Give the extent of all uninfected red blood cells.
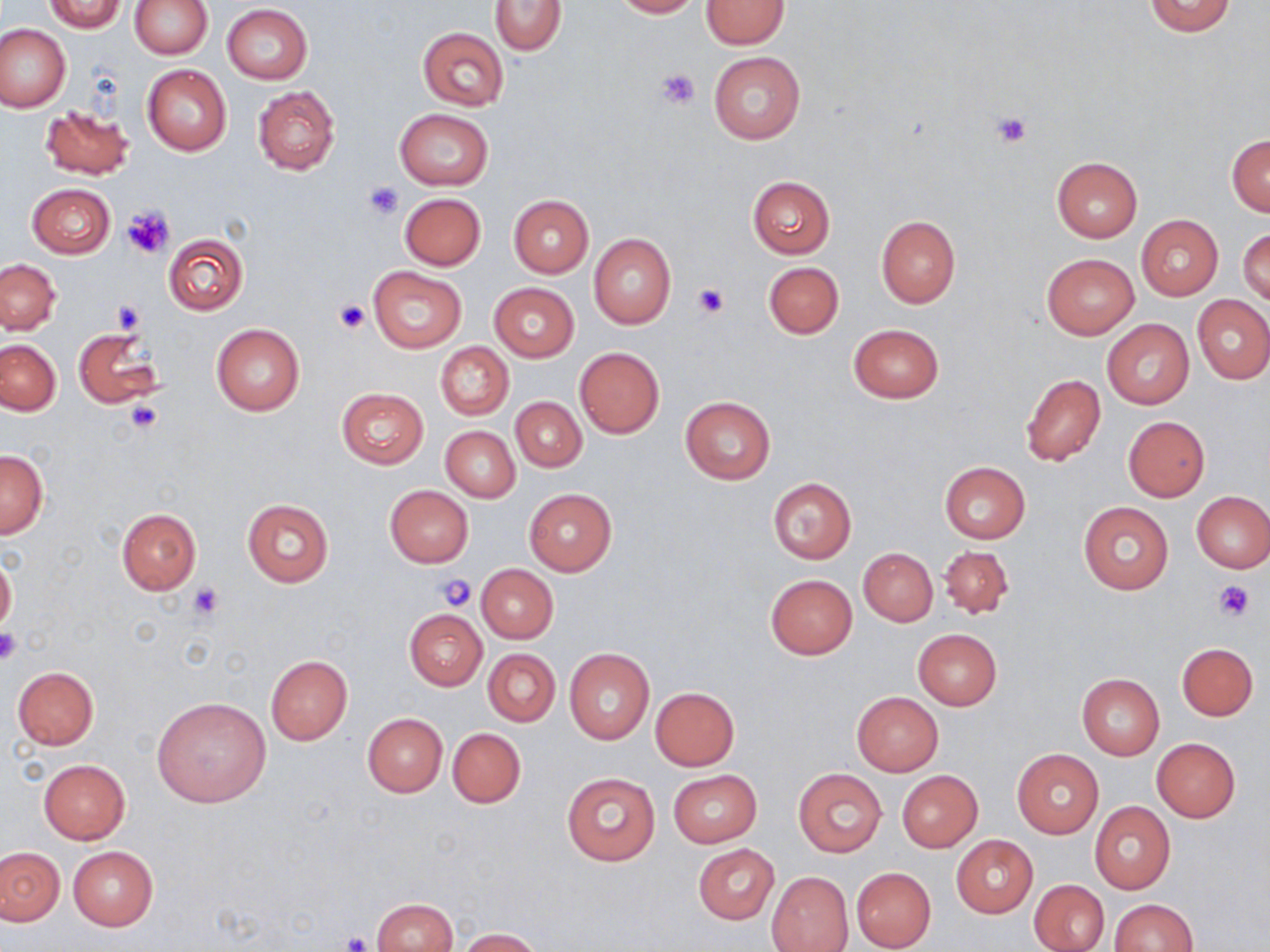
Approximate bounding boxes as (x1,y1)-(x2,y2) corner pairs in pixels.
Uninfected red blood cells: (131,0)-(212,59), (612,0)-(701,18), (40,1)-(126,32), (491,1)-(568,54), (700,1)-(788,49), (1143,1)-(1236,37), (221,4)-(312,84), (0,23)-(70,113), (417,26)-(509,111), (709,52)-(805,145), (142,65)-(232,156), (253,86)-(339,174), (38,104)-(133,182), (394,109)-(493,190), (1227,135)-(1269,216), (1051,157)-(1143,243), (747,176)-(835,259), (27,183)-(114,258), (400,192)-(486,270), (508,194)-(594,277), (1135,215)-(1222,300), (876,216)-(960,309), (1239,226)-(1269,305), (162,233)-(249,316), (588,234)-(676,329), (1042,253)-(1139,339), (1,258)-(61,334), (763,261)-(844,339), (368,266)-(467,352), (489,282)-(579,361), (1193,297)-(1270,384), (1102,319)-(1193,409), (211,323)-(304,416), (848,324)-(945,403), (73,327)-(162,411), (0,340)-(61,414), (434,341)-(513,420), (574,347)-(665,438), (1019,373)-(1106,467), (337,387)-(427,468), (679,396)-(775,484), (511,397)-(586,472), (1122,417)-(1210,501), (441,426)-(519,502), (1,450)-(48,539), (939,462)-(1031,544), (768,478)-(856,563), (385,485)-(473,567), (523,488)-(615,575), (1191,491)-(1270,572), (242,499)-(333,586), (1078,501)-(1173,595), (116,508)-(201,593), (939,545)-(1014,620), (859,547)-(937,627), (0,554)-(16,634), (476,564)-(558,642), (765,574)-(857,659), (404,610)-(486,689), (912,628)-(1001,711), (1177,643)-(1258,720), (483,648)-(560,726), (564,648)-(653,744), (264,655)-(353,745), (12,667)-(99,749), (1077,674)-(1164,759), (649,686)-(740,770), (852,692)-(943,775), (151,696)-(273,808), (361,712)-(447,797), (447,727)-(526,808), (1152,737)-(1239,822), (1012,750)-(1104,839), (38,759)-(130,843), (794,768)-(886,857), (560,770)-(661,866), (669,770)-(762,847), (897,770)-(982,851), (1089,801)-(1175,894), (952,836)-(1037,917), (693,844)-(778,924), (68,846)-(158,929), (1,847)-(64,925), (851,867)-(935,950), (767,871)-(853,951), (1029,879)-(1109,951), (372,897)-(457,952), (1108,900)-(1198,951), (456,928)-(545,952).

Summary:
  - Platelet locations: (656,68)-(700,110), (991,110)-(1033,148), (363,181)-(404,217), (124,206)-(176,259), (693,283)-(728,318), (112,300)-(145,335), (336,300)-(368,333), (125,399)-(164,435), (434,573)-(478,611), (1214,579)-(1255,621), (188,582)-(225,620), (0,629)-(23,666), (340,932)-(372,952)
  - Slide-level diagnosis: negative for blood parasites
  - Field of view: one of a larger specimen
  - Magnification: 1000x
  - Preparation: thin blood smear
  - Image size: 1270×952 pixels
  - Modality: light microscopy
  - Stain: May-Grünwald-Giemsa